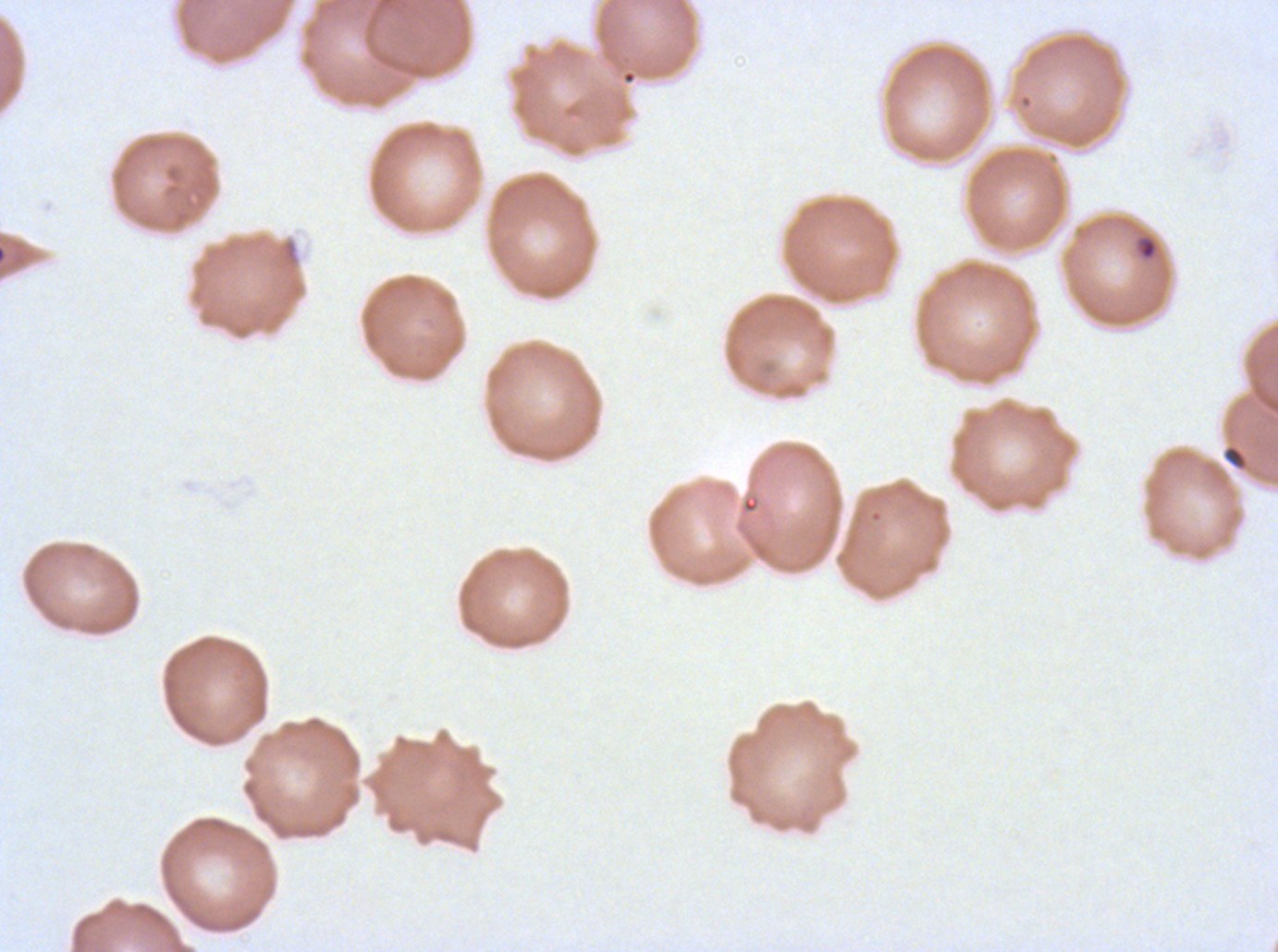
Approximate bounding rectangles given as corner coordinates in pixels from the top-left.
Summary:
  - Ring locations: (x1=1135, y1=234, x2=1159, y2=262)
  - Debris locations: (x1=1223, y1=445, x2=1246, y2=468)
  - Preparation: thin blood film
  - Specimen: ex-vivo Plasmodium falciparum culture from a patient in The Gambia, grown for 24 to 48 hours
  - Stain: Giemsa
  - Image size: 1278×952 pixels
  - Field of view: one sub-image of a larger composite